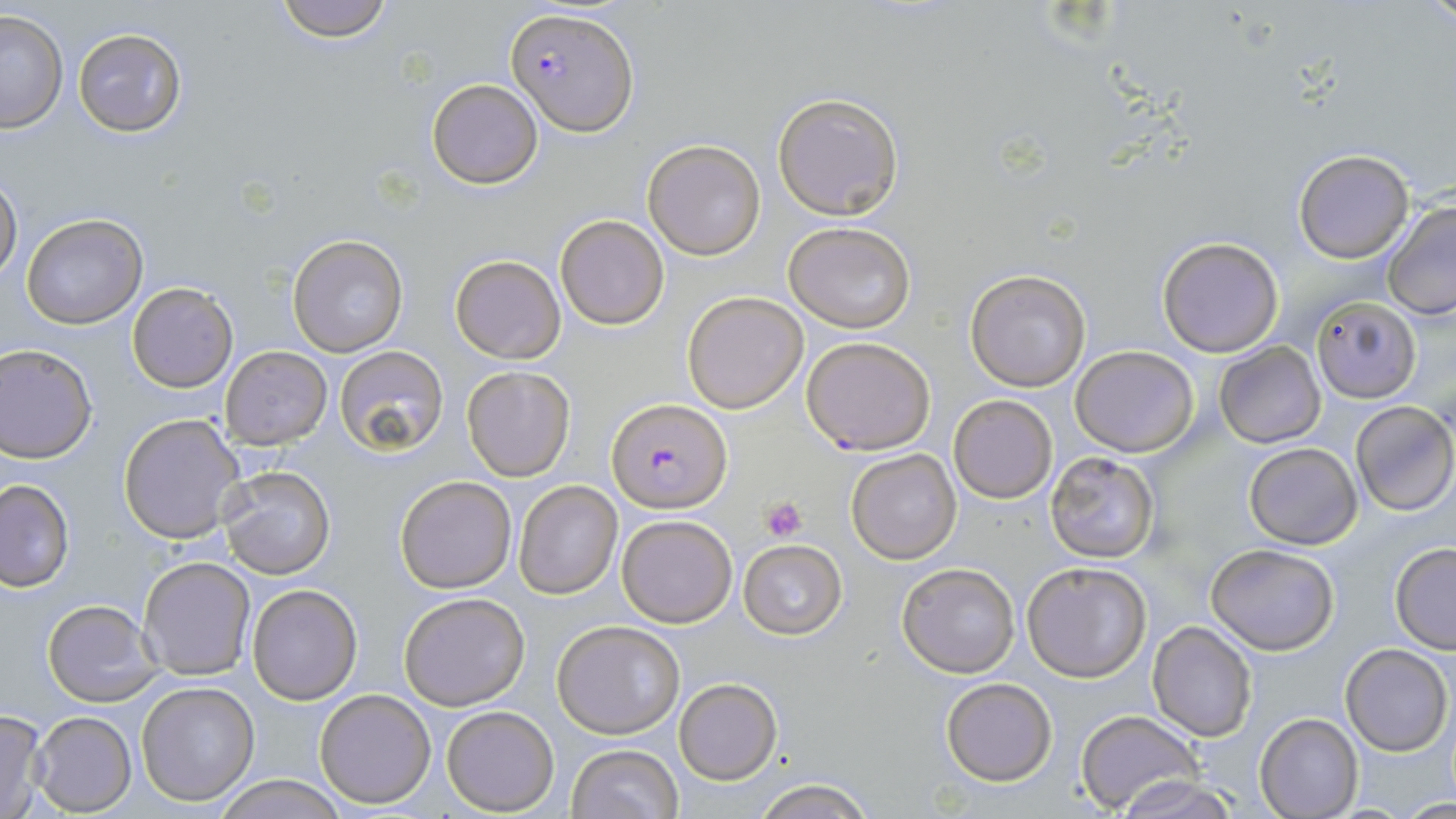
Summary:
  - Coordinate format: approximate bounding boxes as (x1, y1, x2, y2) in pixels
  - Plasmodium falciparum-infected red blood cell locations: (507, 7, 637, 135), (606, 399, 731, 514)
  - Platelet locations: (762, 494, 808, 541)
  - Uninfected red blood cell locations: (269, 0, 401, 44), (1424, 0, 1454, 33), (0, 9, 67, 133), (72, 28, 187, 136), (426, 78, 543, 188), (772, 91, 903, 219), (641, 138, 766, 260), (1293, 147, 1415, 263), (0, 174, 22, 280), (1380, 203, 1456, 321), (20, 212, 146, 330), (555, 213, 671, 331), (784, 221, 917, 333), (288, 234, 409, 357), (1156, 236, 1285, 357), (449, 254, 566, 364), (965, 270, 1091, 391), (127, 283, 237, 392), (682, 291, 808, 413), (1312, 296, 1421, 403), (800, 336, 936, 455), (1214, 341, 1325, 448), (0, 345, 98, 463), (333, 345, 449, 457), (221, 346, 332, 448), (1071, 346, 1199, 457), (462, 365, 576, 481), (949, 394, 1057, 503), (1351, 400, 1456, 516), (118, 412, 246, 544), (1244, 442, 1363, 550), (847, 449, 961, 563), (1044, 451, 1161, 563), (219, 466, 336, 578), (395, 474, 517, 594), (0, 479, 74, 592), (513, 481, 622, 599), (616, 513, 738, 628), (738, 539, 847, 639), (1206, 542, 1341, 655), (1389, 543, 1456, 654), (138, 556, 255, 681), (1021, 561, 1152, 683), (896, 564, 1019, 677), (245, 584, 362, 703), (399, 592, 530, 710), (43, 597, 160, 706), (552, 620, 685, 739), (1147, 621, 1257, 742), (1341, 644, 1452, 755), (940, 677, 1057, 785), (674, 678, 783, 785), (135, 681, 260, 806), (313, 688, 436, 809), (442, 706, 561, 815), (0, 708, 49, 819), (1076, 709, 1203, 815), (30, 710, 136, 815), (1255, 714, 1362, 819), (566, 744, 685, 819), (211, 774, 348, 818), (1115, 775, 1242, 819), (751, 777, 874, 819)
  - Slide-level diagnosis: Plasmodium falciparum
  - Image size: 1456×819 pixels
  - Modality: light microscopy
  - Stain: May-Grünwald-Giemsa
  - Magnification: 1000x
  - Field of view: one of a larger specimen
  - Preparation: thin blood film